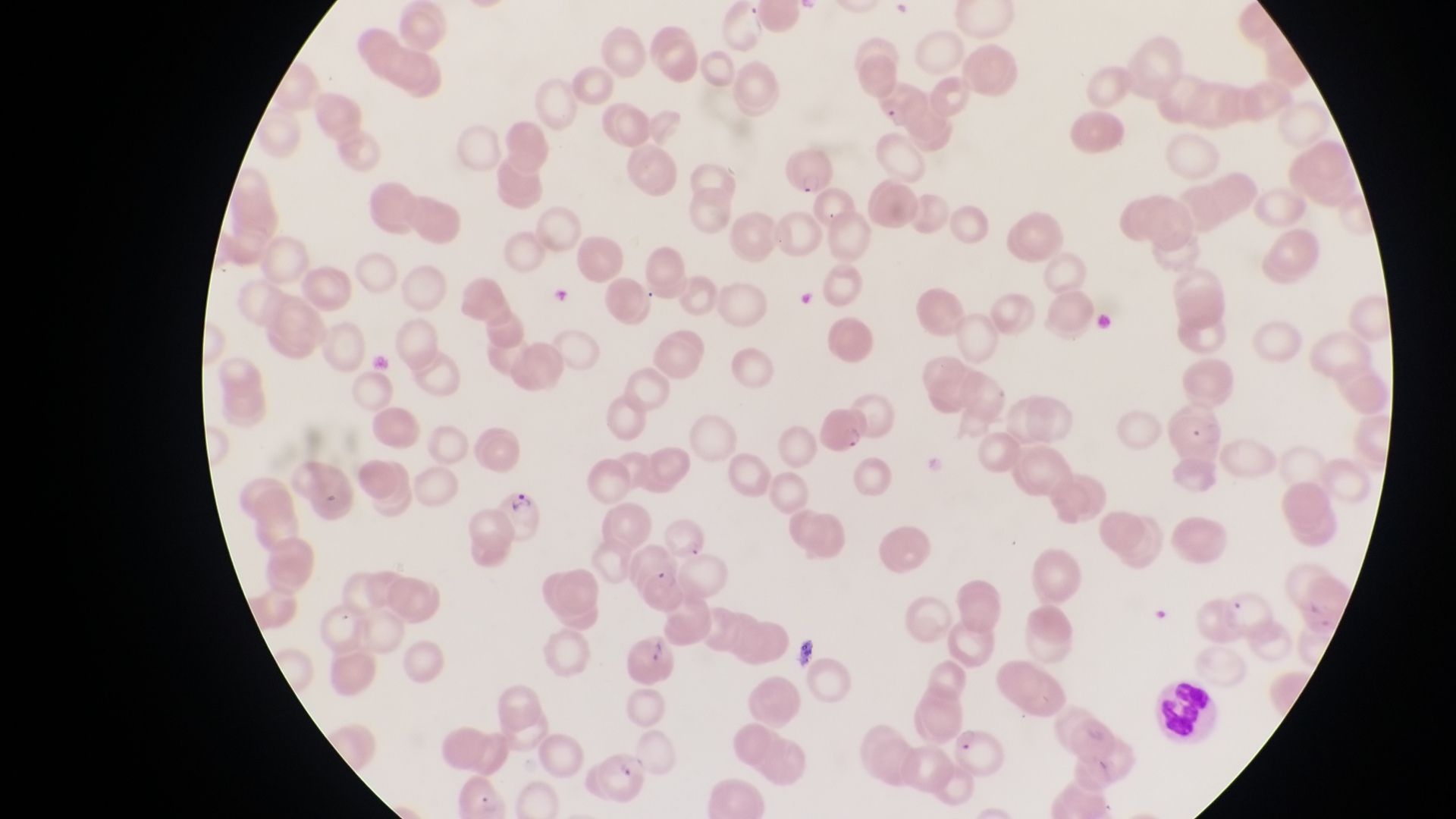
Approximate bounding boxes as [left, top, right, bottom] in pixels.
Summary:
  - Artifact (platelet-like body, stain precipitate, or debris) locations: [792, 632, 824, 666]
  - Parasitised red blood cell locations: [780, 145, 832, 197], [814, 404, 863, 453], [494, 492, 541, 539], [627, 629, 677, 696], [951, 723, 1004, 778], [589, 740, 649, 801]
  - Leukocyte locations: [1152, 671, 1210, 738]
  - Preparation: thin blood film
  - Image size: 1456×819 pixels
  - Field of view: single
  - Country: Uganda
  - Magnification: 1000x
  - Capture: smartphone photograph through the eyepiece of an Olympus CX-23 microscope